Identify the blood parasite species.
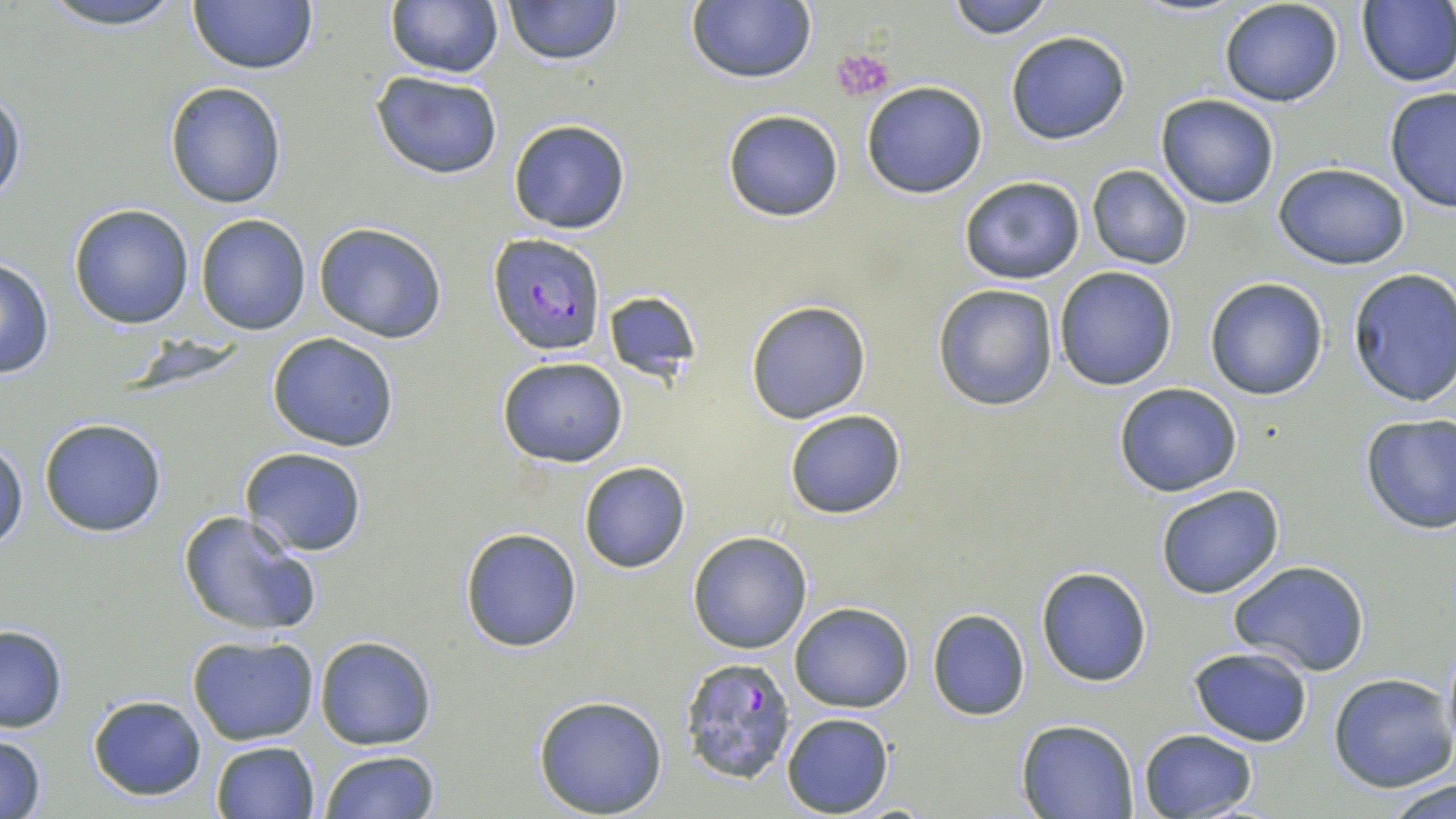

Plasmodium falciparum.

Approximate bounding boxes as (x1, y1, x2, y2) in pixels. Plasmodium falciparum-infected red blood cell locations: (489, 234, 606, 356), (676, 655, 796, 783). Platelet locations: (834, 47, 894, 102). Uninfected red blood cell locations: (32, 0, 193, 30), (503, 0, 621, 65), (686, 0, 815, 84), (943, 0, 1055, 38), (1219, 0, 1345, 107), (1356, 0, 1456, 87), (188, 1, 317, 74), (386, 1, 503, 78), (1004, 29, 1131, 146), (372, 71, 504, 179), (164, 81, 287, 209), (862, 81, 987, 198), (0, 86, 26, 209), (1383, 87, 1456, 212), (1155, 94, 1279, 209), (722, 108, 845, 222), (509, 118, 632, 234), (1273, 162, 1411, 269), (1086, 166, 1193, 269), (958, 174, 1086, 286), (69, 203, 194, 329), (195, 213, 310, 335), (314, 222, 447, 343), (0, 258, 55, 378), (1053, 265, 1179, 391), (1347, 267, 1456, 406), (1205, 277, 1328, 401), (932, 283, 1058, 410), (601, 291, 702, 382), (745, 300, 871, 424), (266, 333, 399, 453), (498, 355, 628, 467), (1113, 382, 1243, 497), (783, 409, 908, 519), (1358, 412, 1456, 533), (39, 418, 166, 537), (1, 441, 26, 552), (241, 447, 369, 555), (578, 462, 690, 573), (1155, 484, 1285, 600), (177, 509, 324, 640), (459, 527, 583, 651), (687, 530, 813, 654), (1227, 561, 1372, 676), (1034, 565, 1152, 688), (790, 602, 913, 712), (926, 609, 1030, 721), (0, 624, 69, 734), (1441, 633, 1456, 761), (186, 635, 319, 746), (314, 635, 435, 750), (1188, 646, 1313, 747), (1328, 675, 1456, 791), (533, 694, 668, 817), (87, 695, 207, 800), (782, 712, 894, 817), (1016, 718, 1140, 819), (1137, 728, 1259, 819), (0, 733, 49, 818), (210, 740, 320, 819), (318, 750, 440, 819), (1383, 773, 1455, 819). Captured at 1000x magnification. May-Grünwald-Giemsa-stained preparation. Optical microscopy. Thin blood smear. One field of a larger specimen. Image is 1456×819 pixels.